Name the parasite shown.
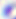

This is Toxoplasma gondii.

Summary:
  - Modality: micrograph
  - Magnification: 400x